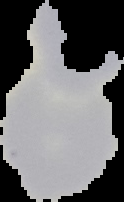

Image is 124×202 pixels. From a thin blood smear. Result: negative for malaria parasites. Cell region segmented out of the field of view; the surrounding area is masked to black.